Assess this cell for malaria.
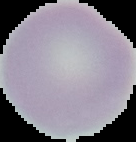
Uninfected.

Segmented cell region on a black background. From a thin blood smear. Image is 136×142 pixels.